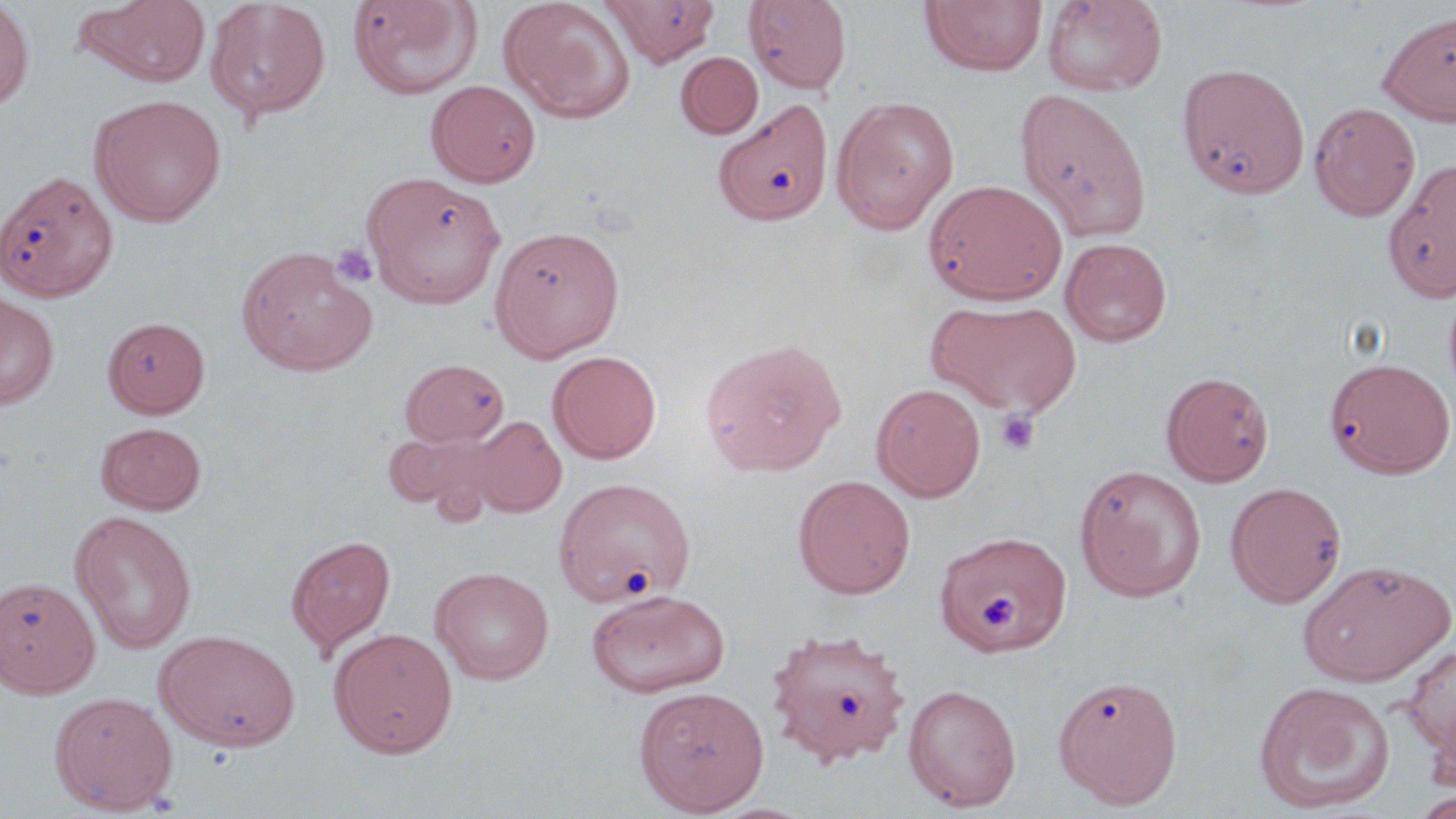

slide-level diagnosis = no evidence of blood parasites
uninfected red blood cell locations = approximate bounding boxes as [x1, y1, x2, y2] in pixels: [0, 0, 34, 112], [75, 0, 213, 87], [206, 0, 332, 122], [347, 0, 483, 99], [498, 0, 636, 123], [602, 0, 721, 66], [743, 0, 852, 93], [920, 0, 1047, 77], [1041, 0, 1167, 96], [1378, 11, 1456, 126], [676, 51, 763, 138], [1178, 63, 1311, 198], [426, 80, 541, 187], [1014, 88, 1152, 240], [89, 94, 227, 227], [830, 96, 959, 234], [713, 98, 834, 226], [1309, 102, 1420, 221], [1383, 159, 1456, 303], [1, 169, 117, 301], [364, 172, 504, 309], [925, 179, 1067, 305], [489, 225, 625, 361], [1061, 237, 1172, 347], [236, 246, 377, 376], [1443, 283, 1456, 403], [0, 292, 59, 409], [930, 299, 1082, 416], [102, 317, 210, 417], [699, 338, 846, 476], [548, 351, 662, 464], [1326, 357, 1455, 478], [400, 359, 509, 446], [1161, 371, 1274, 486], [871, 383, 986, 502], [469, 415, 567, 517], [96, 422, 206, 514], [383, 429, 497, 519], [1074, 464, 1207, 602], [793, 475, 915, 599], [552, 477, 694, 608], [1225, 481, 1347, 608], [70, 510, 197, 654], [934, 531, 1072, 656], [285, 534, 395, 655], [1298, 559, 1454, 687], [430, 566, 555, 685], [0, 577, 100, 698], [586, 589, 731, 698], [765, 626, 911, 767], [329, 627, 458, 759], [155, 629, 300, 751], [1402, 645, 1456, 761], [1052, 673, 1183, 808], [1252, 680, 1395, 814], [902, 683, 1022, 812], [633, 686, 769, 815], [49, 690, 179, 815], [1411, 791, 1456, 818]
field of view = one of a larger specimen
image size = 1456×819 pixels
platelet locations = approximate bounding boxes as [x1, y1, x2, y2] in pixels: [332, 243, 379, 288], [996, 409, 1040, 455]
modality = optical microscopy
magnification = 1000x
preparation = thin blood film
stain = May-Grünwald-Giemsa